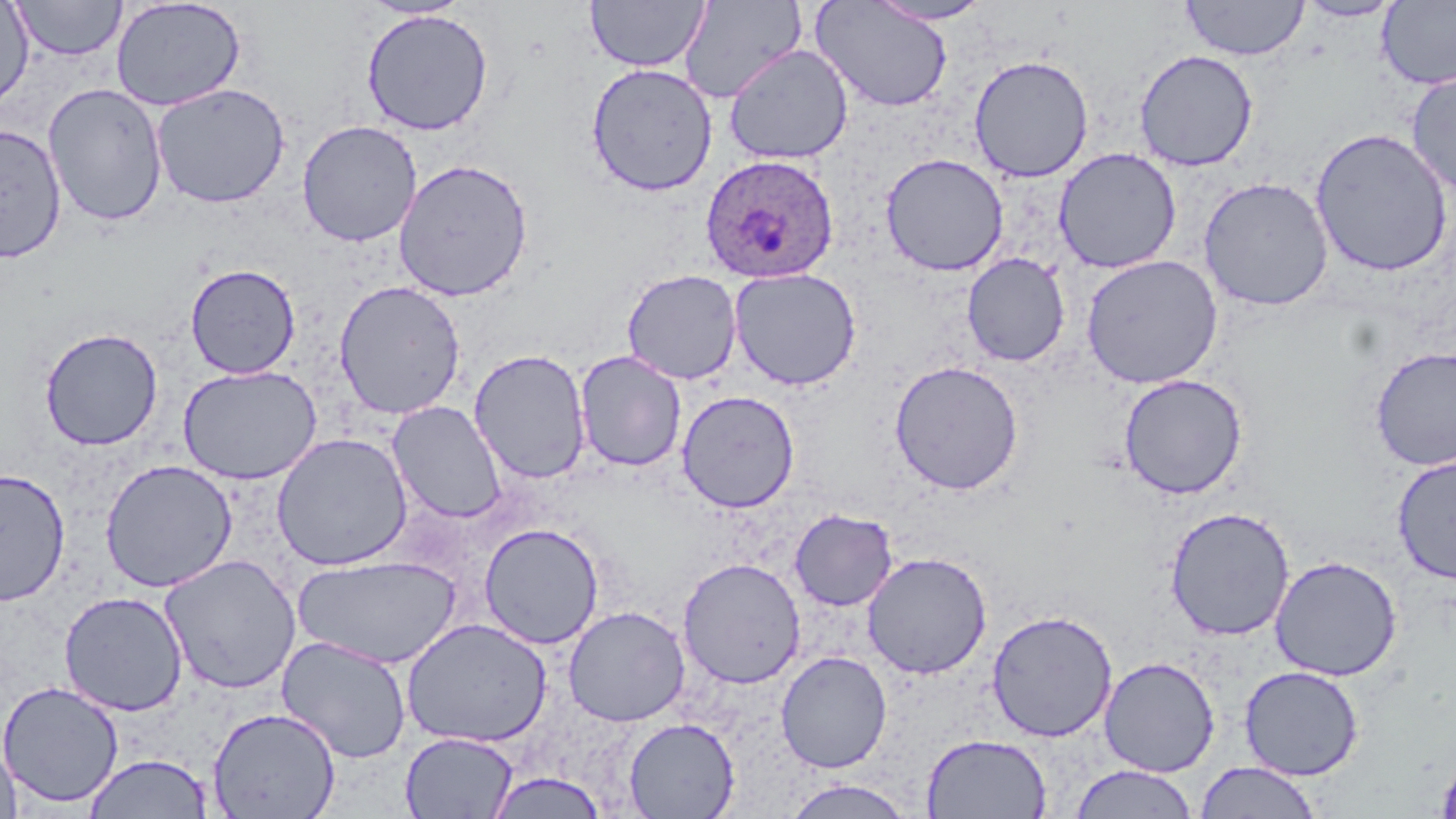

Summary:
  - Coordinate format: approximate bounding boxes as named x1/y1/x2/y2 corners in pixels
  - Plasmodium ovale-infected red blood cell locations: (x1=700, y1=153, x2=840, y2=284)
  - Uninfected red blood cell locations: (x1=585, y1=0, x2=710, y2=72), (x1=678, y1=0, x2=806, y2=104), (x1=867, y1=0, x2=995, y2=25), (x1=1180, y1=0, x2=1309, y2=60), (x1=11, y1=1, x2=127, y2=61), (x1=111, y1=1, x2=247, y2=111), (x1=358, y1=1, x2=476, y2=21), (x1=810, y1=1, x2=954, y2=113), (x1=1294, y1=1, x2=1405, y2=22), (x1=1377, y1=1, x2=1456, y2=89), (x1=0, y1=2, x2=34, y2=113), (x1=361, y1=9, x2=494, y2=136), (x1=724, y1=44, x2=853, y2=164), (x1=1134, y1=49, x2=1259, y2=172), (x1=968, y1=55, x2=1093, y2=182), (x1=586, y1=62, x2=718, y2=197), (x1=1405, y1=72, x2=1456, y2=196), (x1=43, y1=83, x2=168, y2=227), (x1=151, y1=83, x2=290, y2=208), (x1=297, y1=120, x2=422, y2=247), (x1=0, y1=122, x2=67, y2=263), (x1=1310, y1=128, x2=1453, y2=277), (x1=1054, y1=147, x2=1182, y2=273), (x1=880, y1=153, x2=1008, y2=276), (x1=393, y1=158, x2=534, y2=301), (x1=1199, y1=177, x2=1334, y2=311), (x1=961, y1=253, x2=1071, y2=367), (x1=1081, y1=255, x2=1223, y2=389), (x1=185, y1=263, x2=301, y2=379), (x1=728, y1=268, x2=861, y2=390), (x1=621, y1=269, x2=742, y2=385), (x1=333, y1=280, x2=467, y2=419), (x1=40, y1=327, x2=163, y2=450), (x1=1370, y1=346, x2=1456, y2=471), (x1=468, y1=349, x2=592, y2=484), (x1=574, y1=350, x2=687, y2=472), (x1=889, y1=360, x2=1024, y2=495), (x1=178, y1=364, x2=322, y2=485), (x1=1118, y1=373, x2=1248, y2=500), (x1=676, y1=389, x2=800, y2=513), (x1=388, y1=401, x2=506, y2=524), (x1=271, y1=432, x2=413, y2=571), (x1=1392, y1=456, x2=1456, y2=584), (x1=99, y1=459, x2=238, y2=592), (x1=0, y1=468, x2=71, y2=606), (x1=1165, y1=506, x2=1295, y2=641), (x1=789, y1=508, x2=898, y2=611), (x1=479, y1=523, x2=604, y2=649), (x1=861, y1=551, x2=992, y2=679), (x1=160, y1=554, x2=302, y2=694), (x1=293, y1=554, x2=461, y2=669), (x1=1269, y1=555, x2=1402, y2=682), (x1=677, y1=557, x2=806, y2=688), (x1=58, y1=591, x2=188, y2=717), (x1=563, y1=606, x2=690, y2=726), (x1=986, y1=609, x2=1118, y2=742), (x1=401, y1=617, x2=552, y2=747), (x1=277, y1=635, x2=412, y2=763), (x1=775, y1=651, x2=892, y2=773), (x1=1099, y1=656, x2=1220, y2=776), (x1=1239, y1=665, x2=1364, y2=780), (x1=0, y1=680, x2=123, y2=808), (x1=207, y1=707, x2=341, y2=819), (x1=623, y1=717, x2=740, y2=818), (x1=400, y1=732, x2=519, y2=818), (x1=921, y1=733, x2=1051, y2=818), (x1=1, y1=734, x2=22, y2=819), (x1=1435, y1=750, x2=1456, y2=819), (x1=82, y1=753, x2=215, y2=818), (x1=1194, y1=762, x2=1323, y2=818), (x1=1069, y1=764, x2=1199, y2=819), (x1=486, y1=772, x2=607, y2=818), (x1=783, y1=778, x2=915, y2=818)
  - Slide-level diagnosis: Plasmodium ovale
  - Image size: 1456×819 pixels
  - Magnification: 1000x
  - Field of view: single
  - Preparation: thin blood film
  - Modality: light microscopy
  - Stain: May-Grünwald-Giemsa